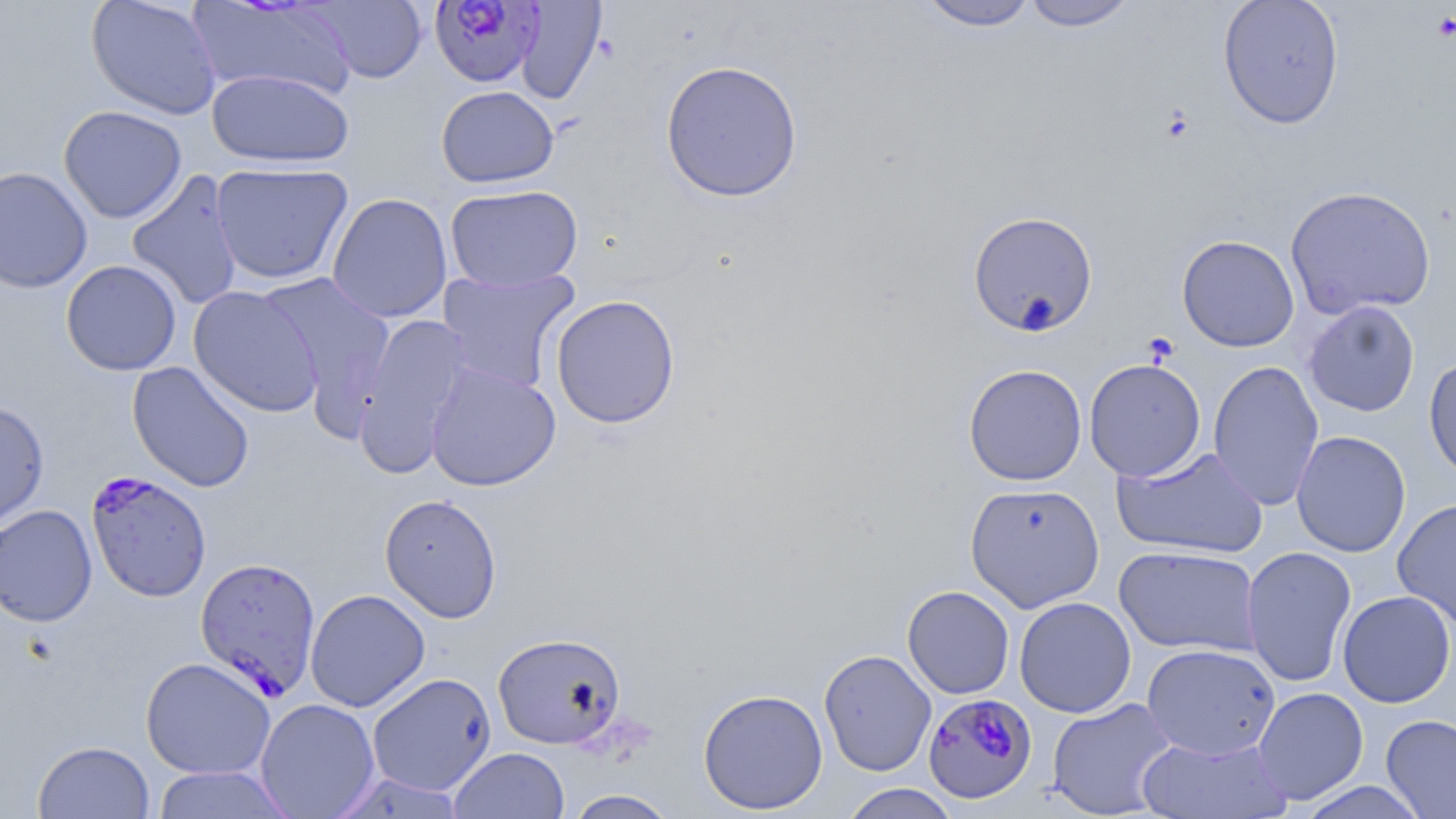

Summary:
  - Coordinate format: approximate bounding boxes as [x1, y1, x2, y2] in pixels
  - Uninfected red blood cell locations: [85, 0, 222, 120], [188, 0, 358, 101], [305, 0, 429, 84], [1019, 0, 1139, 31], [1218, 0, 1344, 129], [514, 1, 607, 105], [916, 1, 1040, 32], [660, 60, 803, 202], [207, 69, 355, 168], [436, 85, 559, 188], [58, 105, 187, 223], [210, 162, 354, 284], [0, 165, 93, 293], [126, 170, 244, 311], [445, 184, 583, 292], [1284, 185, 1436, 320], [326, 192, 453, 323], [967, 210, 1099, 336], [1176, 235, 1300, 352], [60, 259, 182, 376], [438, 268, 580, 393], [256, 273, 395, 420], [188, 286, 324, 418], [550, 294, 681, 429], [1303, 300, 1420, 417], [354, 312, 474, 477], [1423, 355, 1456, 484], [1084, 358, 1206, 481], [1208, 359, 1324, 511], [127, 361, 255, 492], [425, 363, 561, 491], [963, 364, 1087, 486], [0, 400, 50, 534], [1291, 430, 1411, 557], [1111, 446, 1270, 559], [965, 481, 1105, 613], [379, 493, 502, 623], [1392, 498, 1456, 630], [0, 504, 98, 627], [1114, 545, 1262, 657], [1241, 546, 1357, 688], [902, 586, 1015, 699], [304, 589, 430, 712], [1337, 590, 1455, 708], [1014, 596, 1137, 718], [492, 631, 627, 749], [1142, 643, 1280, 760], [819, 649, 937, 776], [140, 657, 276, 779], [366, 672, 496, 796], [1252, 687, 1368, 804], [697, 688, 828, 815], [1046, 697, 1177, 818], [254, 698, 381, 818], [1380, 714, 1456, 818], [1137, 734, 1292, 819], [33, 740, 155, 819], [449, 746, 570, 818], [150, 765, 295, 818], [1295, 781, 1430, 818], [838, 784, 961, 819], [563, 789, 679, 818]
  - Plasmodium falciparum-infected red blood cell locations: [428, 0, 543, 88], [86, 471, 212, 602], [194, 555, 322, 701], [923, 693, 1037, 804]
  - Slide-level diagnosis: Plasmodium falciparum
  - Modality: light microscopy
  - Preparation: thin blood film
  - Field of view: single
  - Magnification: 1000x
  - Image size: 1456×819 pixels
  - Stain: May-Grünwald-Giemsa